Identify the parasite.
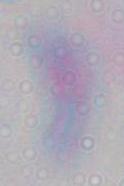

This is Toxoplasma gondii.

1000x magnification. Micrograph.